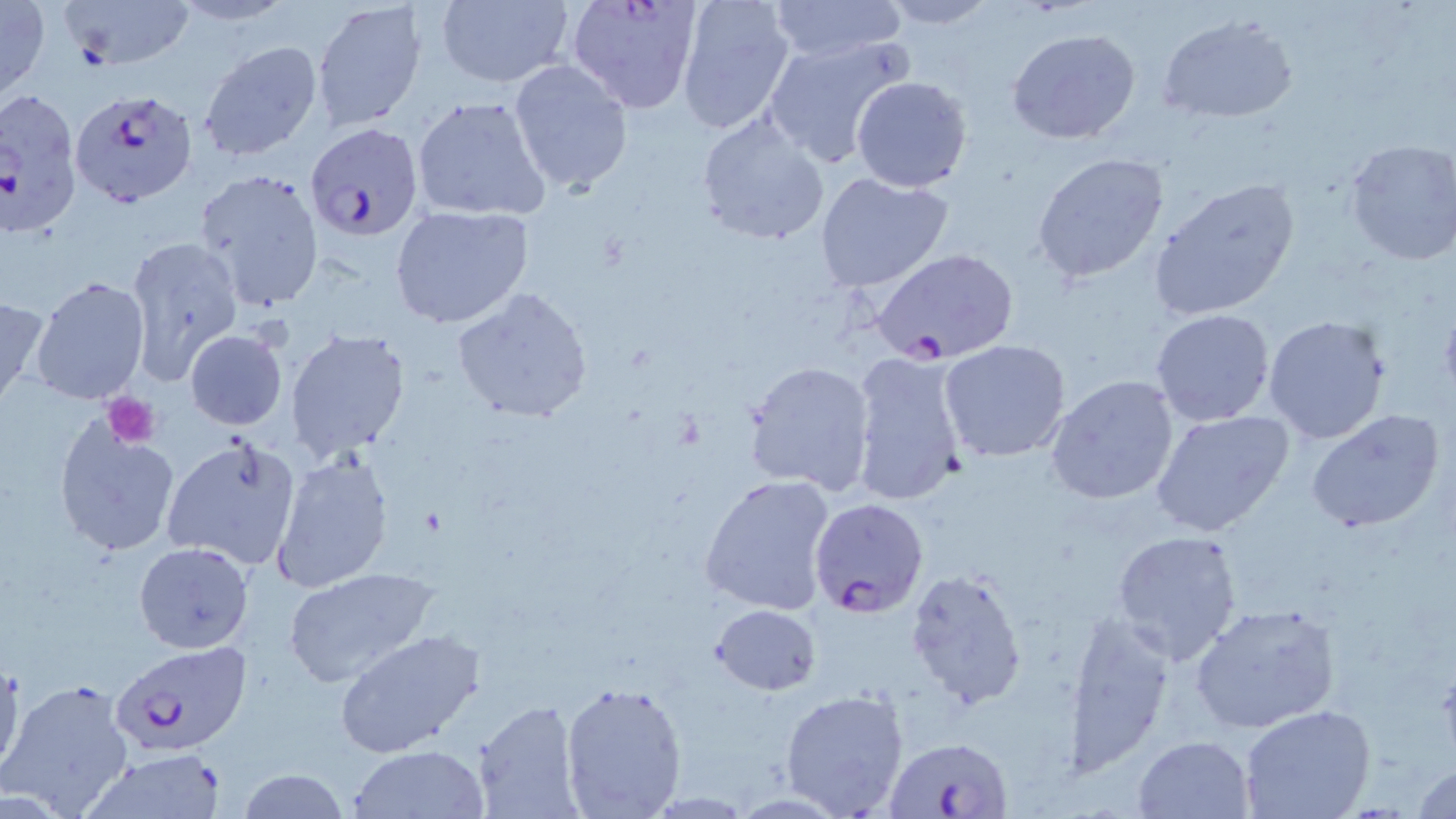

Summary:
  - Coordinate format: approximate bounding boxes as (x1,y1)-(x2,y2) corner pairs in pixels
  - Uninfected red blood cell locations: (0,0)-(50,105), (60,0)-(194,71), (433,0)-(575,89), (675,0)-(797,135), (167,1)-(298,27), (311,1)-(431,134), (763,1)-(910,62), (876,1)-(999,29), (1157,14)-(1298,123), (1007,28)-(1143,146), (761,32)-(913,168), (198,39)-(324,162), (508,59)-(633,193), (849,74)-(973,192), (412,94)-(552,222), (696,113)-(831,246), (1344,138)-(1456,266), (1032,152)-(1170,283), (195,168)-(325,311), (814,171)-(955,294), (1149,177)-(1301,321), (390,204)-(533,328), (123,233)-(243,383), (29,274)-(151,404), (453,287)-(594,424), (0,292)-(48,412), (1150,308)-(1277,426), (1263,313)-(1392,444), (285,328)-(409,462), (184,329)-(288,429), (940,338)-(1073,463), (847,349)-(972,508), (744,359)-(876,494), (1044,376)-(1181,505), (1149,408)-(1294,537), (1304,408)-(1447,535), (51,417)-(182,556), (161,434)-(301,573), (269,453)-(396,592), (699,475)-(838,617), (1111,529)-(1245,664), (134,542)-(255,653), (280,565)-(442,688), (905,569)-(1028,711), (709,601)-(821,695), (1190,604)-(1340,734), (1061,611)-(1176,769), (336,630)-(485,759), (0,656)-(26,781), (2,675)-(137,818), (560,678)-(688,818), (780,687)-(911,818), (475,700)-(585,819), (1239,706)-(1376,819), (1133,736)-(1255,818), (349,745)-(490,818), (79,750)-(227,818), (1412,762)-(1456,819), (237,768)-(350,819)
  - Platelet locations: (104,393)-(161,449)
  - Plasmodium falciparum-infected red blood cell locations: (564,0)-(706,113), (70,88)-(197,207), (0,89)-(82,238), (304,123)-(426,244), (868,246)-(1019,365), (808,497)-(929,620), (109,639)-(252,756), (884,736)-(1018,818)
  - Slide-level diagnosis: Plasmodium falciparum
  - Modality: optical microscopy
  - Image size: 1456×819 pixels
  - Preparation: thin blood smear
  - Magnification: 1000x
  - Field of view: one of a larger specimen
  - Stain: May-Grünwald-Giemsa